State which parasite is depicted.
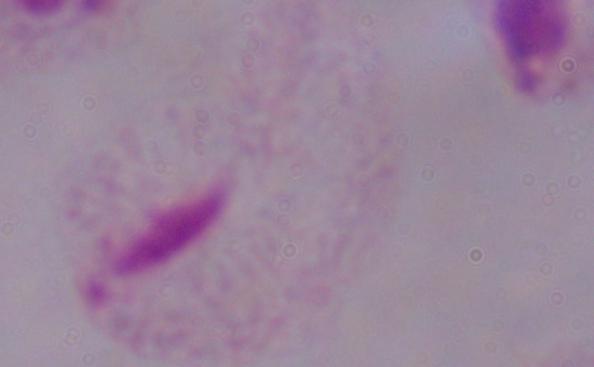
This is a trichomonad.

modality: photomicrograph
magnification: 1000x